Assess this cell for malaria.
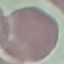

Uninfected.

Photographed with a smartphone camera at the microscope eyepiece. Giemsa stain. Thin blood smear. Automatically extracted cell patch, resized to 64 × 64 pixels.